Assess the morphology of the erythrocytes.
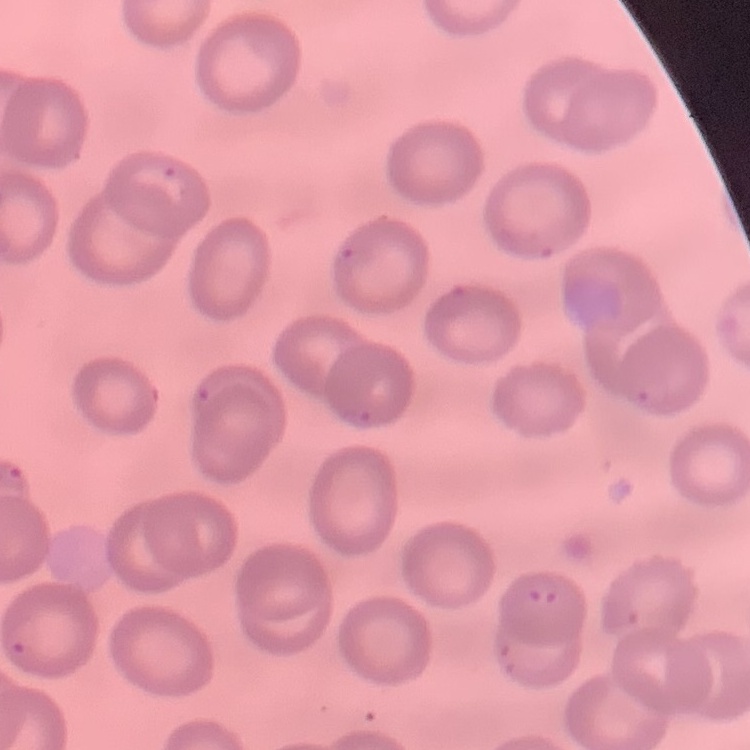

No rouleaux formation.

preparation = thin blood smear
image type = square crop of a larger photomicrograph
stain = Field's or Giemsa